Locate every blood parasite and identify its species.
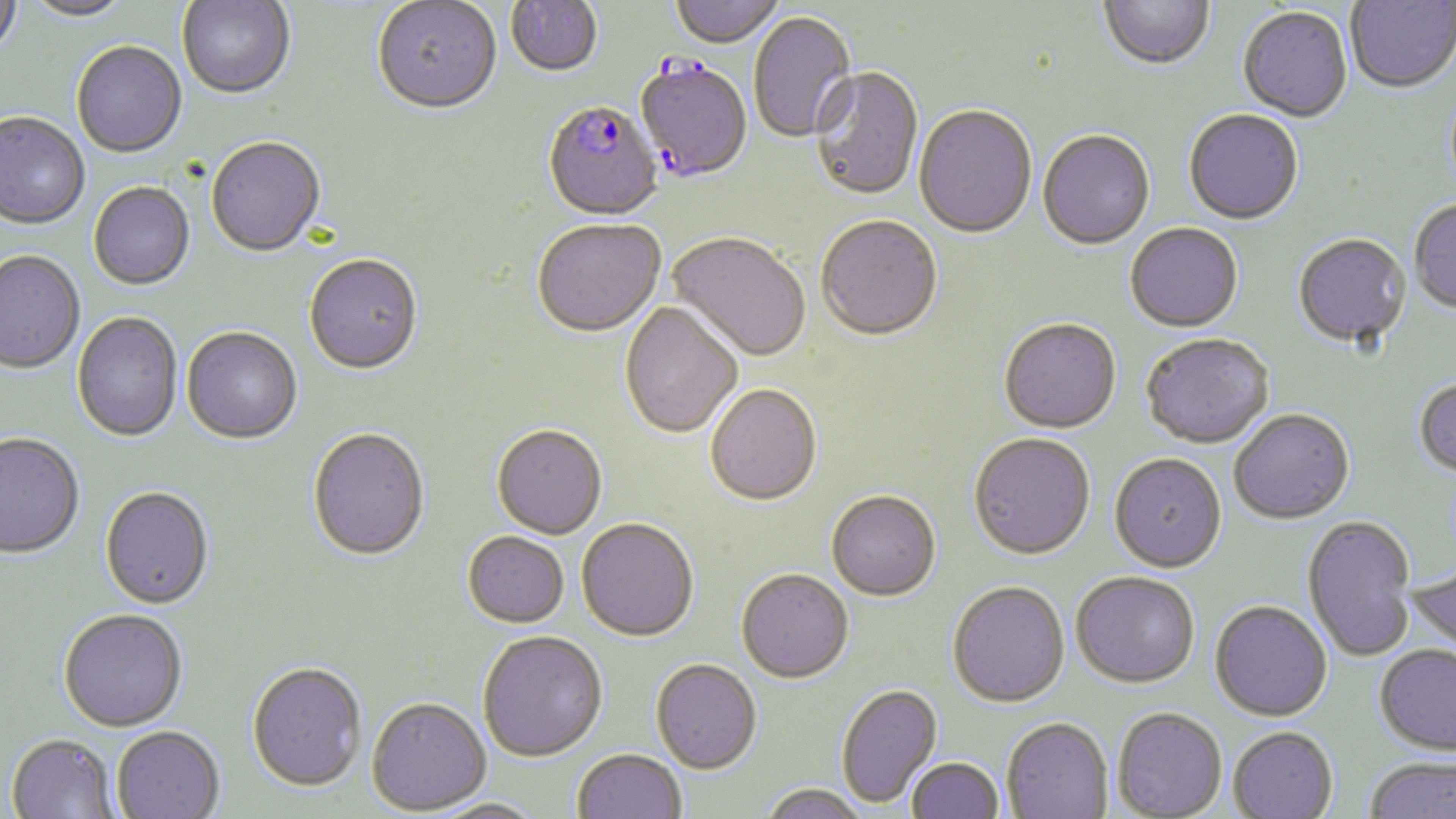
Approximate bounding boxes as named x1/y1/x2/y2 corners in pixels.
Plasmodium falciparum-infected red blood cells: (x1=633, y1=59, x2=753, y2=185), (x1=543, y1=103, x2=663, y2=223).
No Plasmodium ovale, Plasmodium malariae, Plasmodium vivax, Babesia divergens, or Trypanosoma brucei observed.

Uninfected red blood cell locations: (x1=0, y1=0, x2=23, y2=62), (x1=670, y1=0, x2=784, y2=50), (x1=1100, y1=0, x2=1214, y2=73), (x1=1345, y1=0, x2=1456, y2=95), (x1=21, y1=1, x2=134, y2=23), (x1=177, y1=1, x2=296, y2=102), (x1=372, y1=1, x2=502, y2=118), (x1=506, y1=1, x2=603, y2=79), (x1=1238, y1=8, x2=1353, y2=124), (x1=749, y1=12, x2=857, y2=145), (x1=72, y1=43, x2=187, y2=160), (x1=810, y1=68, x2=924, y2=203), (x1=914, y1=106, x2=1037, y2=241), (x1=1183, y1=111, x2=1303, y2=227), (x1=0, y1=114, x2=90, y2=232), (x1=1038, y1=131, x2=1155, y2=251), (x1=206, y1=139, x2=325, y2=259), (x1=89, y1=184, x2=195, y2=293), (x1=1409, y1=200, x2=1456, y2=315), (x1=816, y1=218, x2=942, y2=344), (x1=532, y1=221, x2=666, y2=340), (x1=1125, y1=224, x2=1243, y2=334), (x1=667, y1=234, x2=810, y2=365), (x1=1293, y1=235, x2=1411, y2=349), (x1=0, y1=253, x2=85, y2=376), (x1=304, y1=257, x2=423, y2=377), (x1=619, y1=303, x2=743, y2=440), (x1=72, y1=313, x2=183, y2=443), (x1=999, y1=320, x2=1122, y2=436), (x1=182, y1=329, x2=302, y2=447), (x1=1140, y1=334, x2=1274, y2=450), (x1=1413, y1=377, x2=1456, y2=478), (x1=705, y1=386, x2=823, y2=509), (x1=1229, y1=408, x2=1355, y2=525), (x1=491, y1=427, x2=607, y2=541), (x1=308, y1=430, x2=430, y2=564), (x1=0, y1=435, x2=84, y2=561), (x1=968, y1=435, x2=1095, y2=562), (x1=1110, y1=454, x2=1227, y2=573), (x1=100, y1=488, x2=214, y2=611), (x1=826, y1=493, x2=941, y2=602), (x1=1302, y1=515, x2=1417, y2=663), (x1=576, y1=520, x2=699, y2=643), (x1=462, y1=533, x2=570, y2=631), (x1=1407, y1=566, x2=1456, y2=661), (x1=736, y1=570, x2=854, y2=685), (x1=1070, y1=571, x2=1200, y2=689), (x1=947, y1=582, x2=1070, y2=709), (x1=1209, y1=599, x2=1332, y2=721), (x1=59, y1=610, x2=189, y2=734), (x1=478, y1=633, x2=608, y2=763), (x1=1374, y1=644, x2=1456, y2=756), (x1=650, y1=660, x2=762, y2=774), (x1=246, y1=664, x2=367, y2=794), (x1=836, y1=684, x2=942, y2=808), (x1=367, y1=698, x2=492, y2=816), (x1=1112, y1=706, x2=1227, y2=818), (x1=1002, y1=717, x2=1113, y2=818), (x1=1228, y1=726, x2=1338, y2=819), (x1=112, y1=727, x2=225, y2=818), (x1=6, y1=735, x2=120, y2=818), (x1=572, y1=749, x2=686, y2=819), (x1=907, y1=757, x2=1004, y2=818), (x1=1363, y1=757, x2=1455, y2=818), (x1=760, y1=782, x2=868, y2=819), (x1=428, y1=799, x2=547, y2=818). Slide-level diagnosis: Plasmodium falciparum. May-Grünwald-Giemsa-stained preparation. One field of a larger specimen. Captured at 1000x magnification. Thin blood smear. Image is 1456×819 pixels. Optical microscopy.